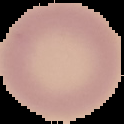

Summary:
  - Image size: 124×124 pixels
  - Result: no malaria parasites seen
  - Preparation: thin blood film
  - Image type: cell region segmented out of the field of view; surrounding area masked to black